State which parasite is depicted.
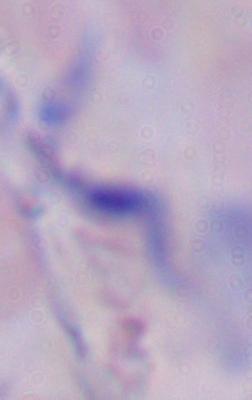

A trypanosome.

Captured at 1000x magnification. Micrograph.